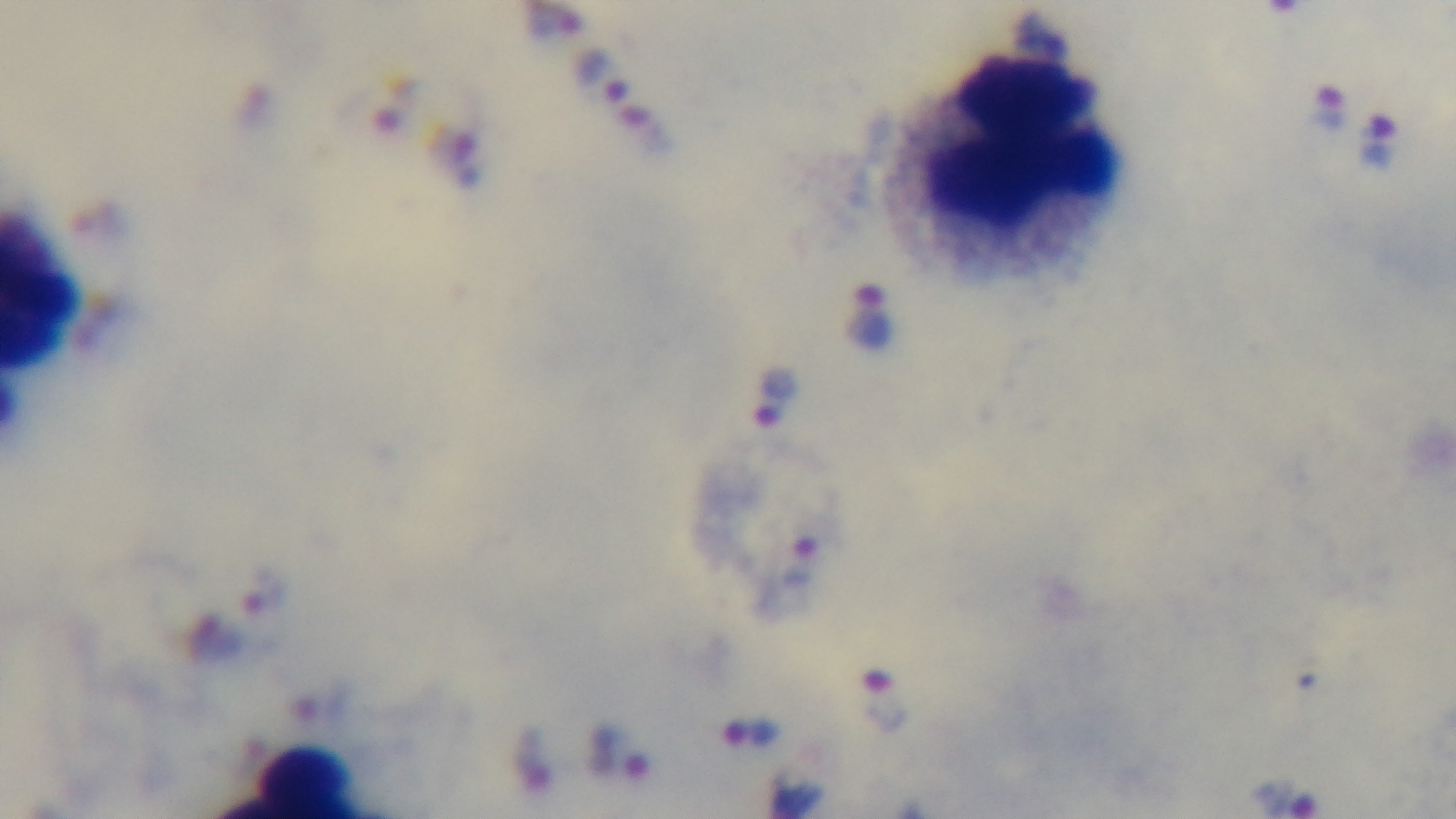

Summary:
  - Malaria status: positive
  - Preparation: thick blood film
  - Capture: mounted 4K digital camera
  - Objective: 100x oil immersion
  - Stain: Giemsa
  - Field of view: one from the slide
  - Modality: light microscopy